Name the parasite shown.
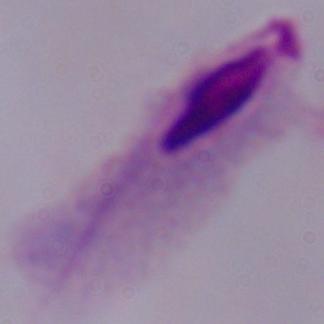
A trichomonad.

Summary:
  - Modality: micrograph
  - Magnification: 1000x